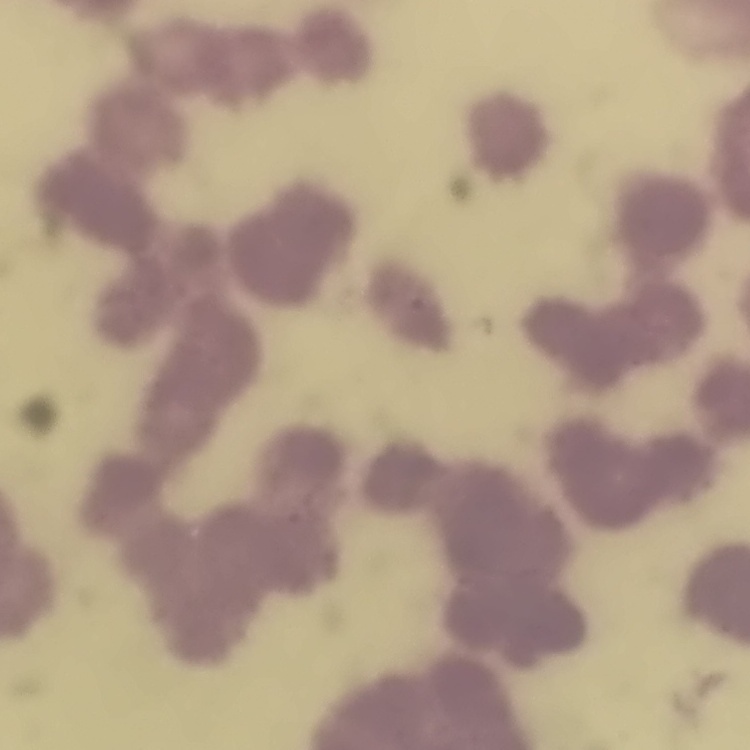
Summary:
  - Red blood cell morphology: rouleaux formation
  - Preparation: thin peripheral smear
  - Image type: square crop of a larger photomicrograph
  - Stain: Field's or Giemsa